Outline each blood parasite and name the species.
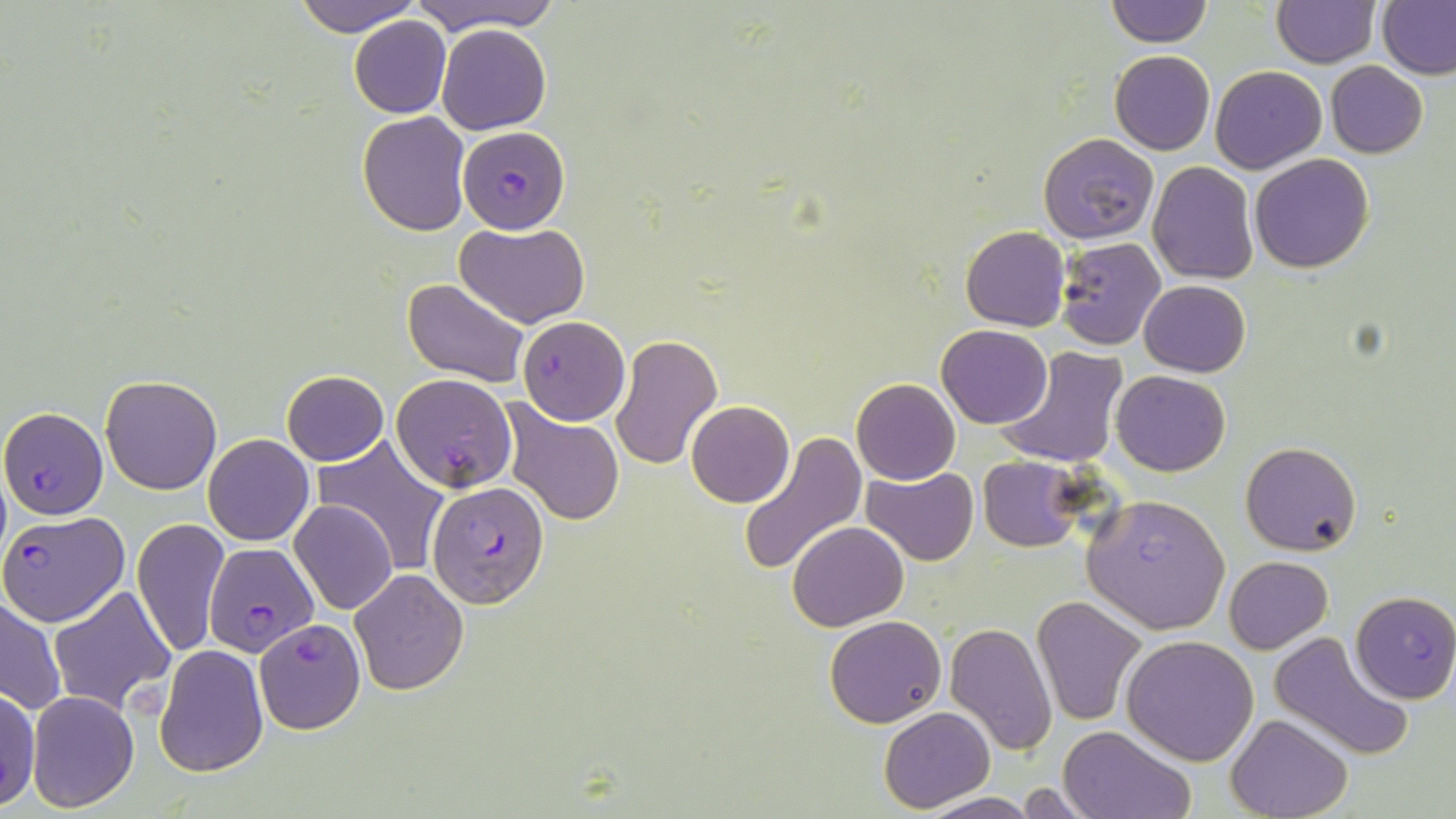
Approximate bounding boxes as (x1, y1, x2, y2) in pixels.
Plasmodium falciparum-infected red blood cells: (458, 125, 568, 233), (517, 316, 629, 425), (392, 372, 516, 493), (2, 406, 108, 519), (426, 482, 549, 609), (1082, 493, 1231, 634), (1, 510, 131, 626), (204, 542, 318, 656), (1350, 591, 1456, 703).
No Plasmodium ovale, Plasmodium malariae, Plasmodium vivax, Babesia divergens, or Trypanosoma brucei observed.

Uninfected red blood cell locations: (294, 0, 421, 35), (406, 0, 566, 36), (1105, 1, 1214, 48), (1271, 1, 1377, 67), (1377, 1, 1456, 80), (349, 15, 451, 118), (437, 23, 551, 134), (1110, 50, 1215, 155), (1326, 62, 1428, 157), (1211, 65, 1326, 174), (356, 112, 471, 236), (1039, 133, 1160, 243), (1250, 153, 1375, 273), (1148, 161, 1260, 284), (456, 222, 587, 329), (961, 226, 1071, 331), (1055, 237, 1166, 351), (401, 277, 529, 386), (1140, 279, 1250, 377), (937, 325, 1052, 429), (609, 333, 723, 470), (995, 346, 1129, 471), (280, 369, 390, 465), (1111, 370, 1231, 475), (101, 375, 221, 495), (851, 378, 960, 485), (686, 400, 795, 508), (503, 404, 626, 526), (204, 434, 314, 545), (740, 435, 866, 574), (312, 438, 449, 576), (1241, 440, 1361, 556), (980, 456, 1084, 551), (862, 467, 980, 564), (289, 500, 399, 614), (132, 516, 229, 658), (788, 521, 909, 630), (1224, 556, 1333, 654), (349, 569, 469, 695), (49, 585, 176, 715), (1, 595, 67, 714), (1032, 596, 1146, 726), (824, 614, 946, 728), (255, 618, 365, 735), (944, 621, 1057, 756), (1265, 630, 1416, 763), (1120, 634, 1260, 765), (155, 644, 268, 776), (0, 686, 39, 809), (26, 691, 140, 810), (880, 707, 995, 812), (1226, 715, 1351, 819), (1059, 727, 1194, 819), (1012, 783, 1103, 817), (921, 791, 1038, 819). Slide-level diagnosis: Plasmodium falciparum. May-Grünwald-Giemsa stain. Thin blood smear. Image is 1456×819 pixels. One field of a larger specimen. Captured at 1000x magnification. Optical microscopy.